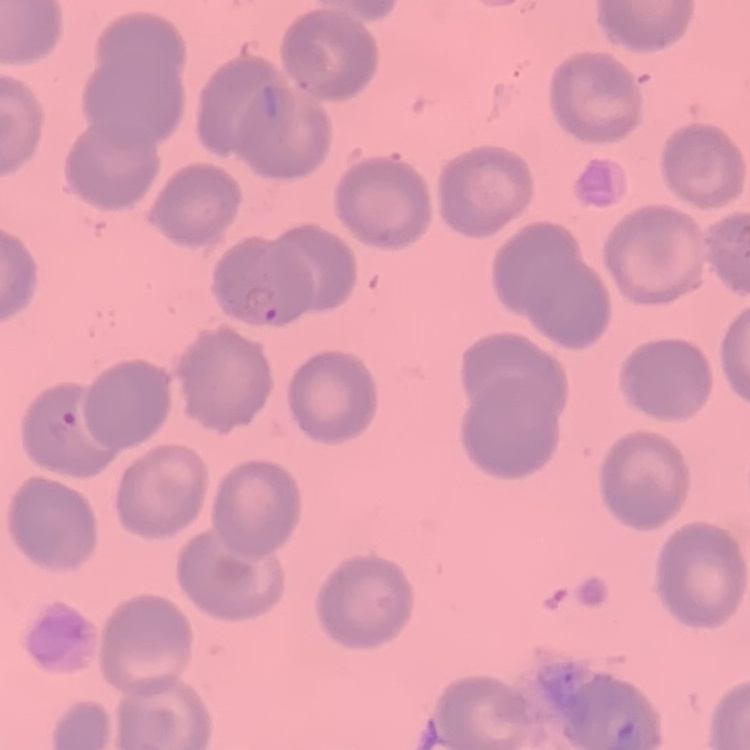

Summary:
  - Red blood cell morphology: no rouleaux formation
  - Image type: square crop of a larger photomicrograph
  - Preparation: thin blood film
  - Stain: Field's or Giemsa